Locate and identify every blood parasite.
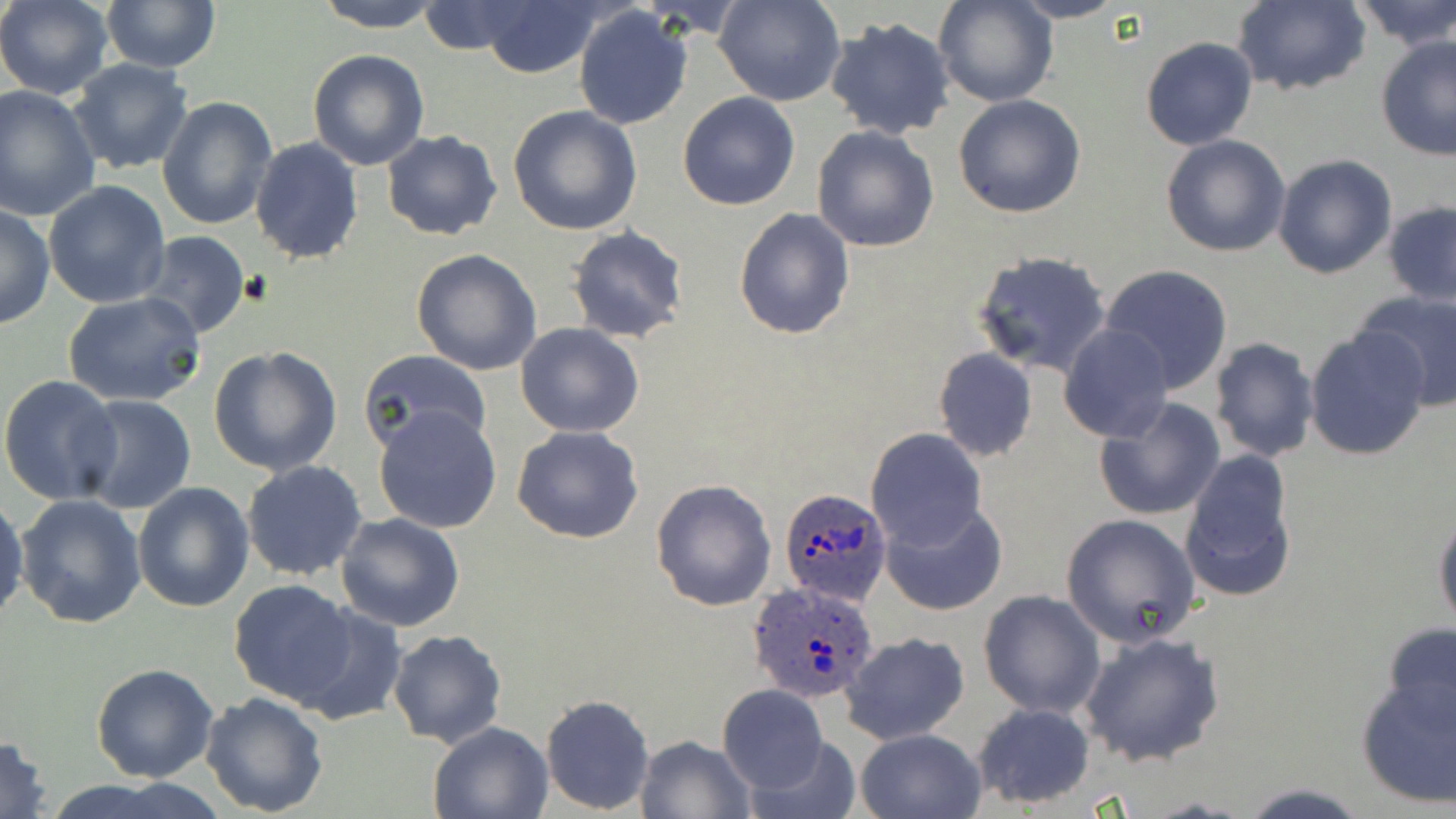

Approximate bounding boxes as [x1, y1, x2, y2] in pixels.
Plasmodium ovale-infected red blood cells: [779, 488, 894, 607], [746, 580, 883, 702].
No Plasmodium falciparum, Plasmodium malariae, Plasmodium vivax, Babesia divergens, or Trypanosoma brucei observed.

Uninfected red blood cell locations: [0, 0, 113, 98], [100, 0, 220, 72], [314, 0, 445, 32], [716, 0, 844, 106], [934, 0, 1055, 107], [1009, 0, 1127, 23], [1348, 0, 1456, 49], [472, 1, 604, 79], [1232, 1, 1370, 96], [418, 2, 525, 55], [573, 5, 693, 130], [824, 16, 956, 140], [1375, 34, 1456, 160], [1139, 37, 1258, 151], [308, 48, 430, 171], [68, 58, 193, 175], [0, 85, 101, 222], [677, 92, 801, 210], [953, 93, 1087, 218], [156, 95, 277, 232], [508, 104, 643, 234], [811, 124, 940, 254], [382, 130, 503, 241], [1160, 134, 1291, 258], [249, 137, 365, 265], [1272, 154, 1396, 279], [44, 182, 170, 308], [1383, 201, 1456, 306], [0, 203, 54, 330], [734, 207, 856, 339], [566, 226, 691, 345], [134, 232, 252, 340], [411, 249, 543, 376], [971, 250, 1111, 377], [1098, 264, 1237, 395], [1354, 289, 1456, 407], [63, 291, 206, 407], [515, 322, 645, 438], [1060, 324, 1173, 442], [1305, 326, 1431, 460], [1208, 337, 1320, 463], [209, 346, 343, 476], [933, 348, 1039, 462], [359, 349, 492, 456], [0, 375, 120, 504], [74, 395, 196, 513], [1094, 398, 1226, 522], [373, 404, 503, 533], [512, 425, 644, 544], [866, 429, 986, 551], [1178, 450, 1299, 603], [241, 460, 368, 582], [651, 478, 778, 612], [132, 482, 254, 613], [0, 493, 27, 625], [16, 494, 147, 629], [880, 499, 1007, 615], [1432, 505, 1456, 628], [336, 512, 464, 633], [1059, 513, 1202, 649], [229, 579, 359, 706], [978, 590, 1107, 718], [290, 602, 407, 724], [1381, 622, 1456, 732], [387, 629, 506, 748], [1078, 629, 1226, 768], [839, 631, 969, 746], [92, 664, 219, 782], [1354, 674, 1455, 808], [717, 685, 828, 794], [199, 691, 330, 815], [539, 694, 655, 816], [971, 701, 1097, 809], [428, 721, 555, 818], [854, 727, 987, 819], [0, 734, 53, 819], [634, 734, 756, 819], [746, 735, 864, 819], [1236, 782, 1372, 817]. Slide-level diagnosis: Plasmodium ovale. Image is 1456×819 pixels. Thin blood film. Captured at 1000x magnification. Light microscopy. One field of a larger specimen. May-Grünwald-Giemsa stain.